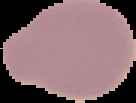
Summary:
  - Image type: segmented cell region on a black background
  - Result: no malaria parasites seen
  - Preparation: thin blood film
  - Image size: 136×103 pixels